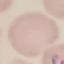
Summary:
  - Result: malaria parasites identified
  - Stain: Giemsa
  - Image type: automatically extracted cell patch, resized to 64 × 64 pixels
  - Preparation: thin smear
  - Capture: smartphone through the microscope eyepiece